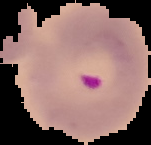
Cell region segmented out of the field of view; the surrounding area is masked to black. Malaria status: parasitized. From a thin blood smear. Image is 151×145 pixels.